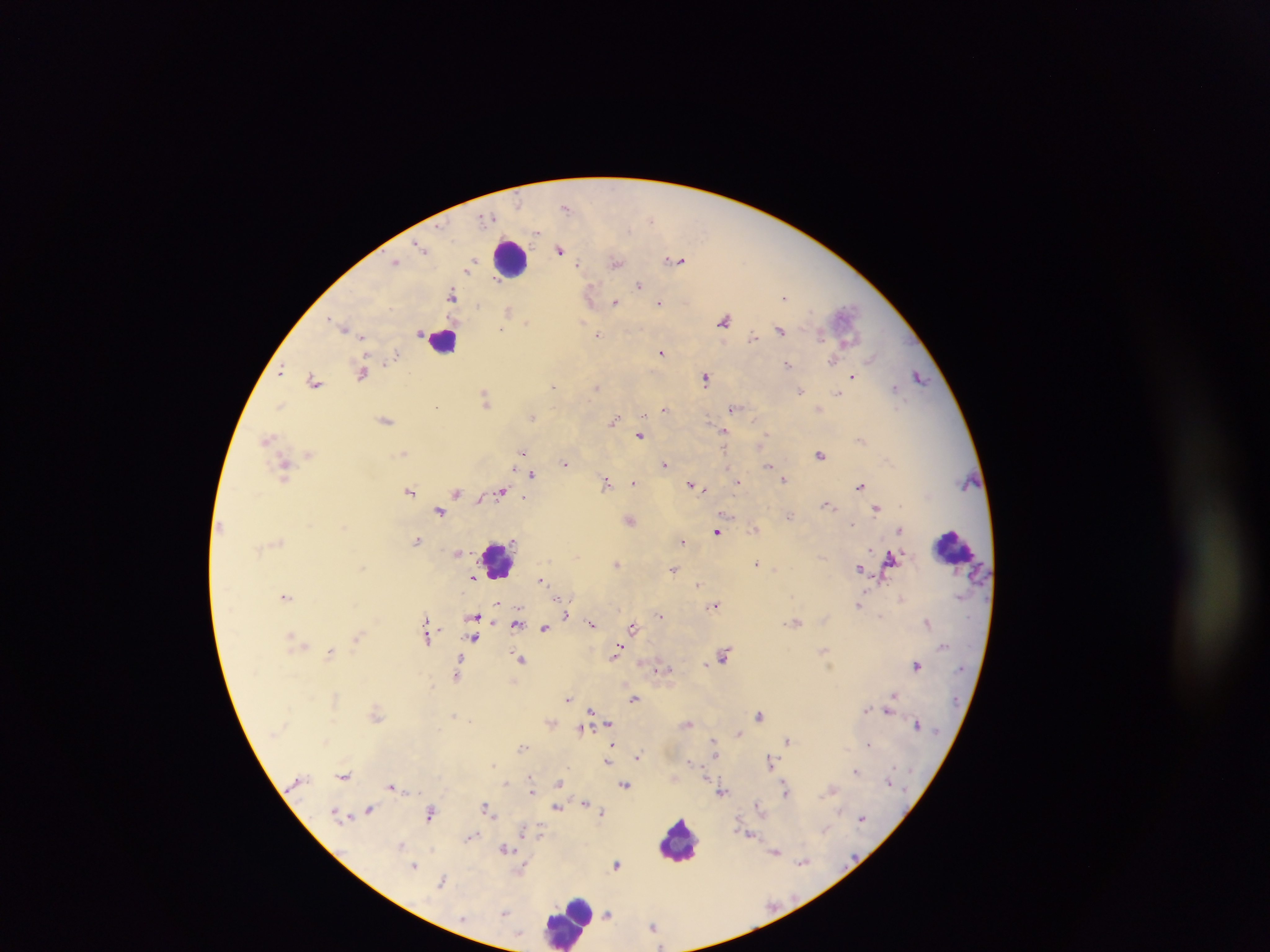

Approximate centers as [x, y] in pixels.
Summary:
  - Leukocyte locations: [510, 258], [442, 340], [953, 546], [500, 558], [680, 840], [567, 920]
  - Plasmodium parasite locations: [566, 207], [487, 216], [651, 219], [537, 233], [421, 247], [560, 250], [679, 261], [396, 262], [472, 262], [616, 262], [578, 264], [468, 270], [638, 285], [453, 295], [785, 296], [615, 302], [659, 302], [476, 305], [508, 311], [725, 320], [526, 322], [505, 323], [344, 327], [501, 329], [780, 330], [597, 334], [753, 336], [362, 337], [821, 337], [661, 352], [395, 355], [871, 359], [390, 360], [833, 361], [788, 364], [281, 371], [362, 373], [852, 376], [919, 376], [706, 378], [315, 381], [553, 387], [597, 387], [895, 388], [801, 390], [838, 393], [485, 396], [281, 405], [437, 405], [733, 407], [664, 409], [645, 416], [533, 417], [385, 420], [613, 421], [724, 432], [640, 435], [765, 437], [268, 438], [860, 440], [404, 453], [523, 453], [309, 454], [820, 454], [565, 462], [665, 464], [769, 466], [284, 469], [532, 474], [784, 479], [738, 481], [606, 483], [634, 483], [692, 485], [859, 485], [704, 489], [410, 491], [501, 491], [457, 493], [525, 497], [827, 504], [876, 507], [440, 512], [790, 515], [630, 520], [851, 524], [755, 528], [900, 529], [716, 531], [417, 540], [682, 541], [890, 560], [757, 563], [617, 564], [364, 566], [859, 568], [673, 569], [473, 577], [540, 580], [698, 584], [286, 596], [558, 600], [499, 604], [715, 604], [859, 604], [660, 614], [474, 616], [566, 616], [882, 617], [427, 620], [928, 622], [517, 623], [591, 623], [633, 627], [545, 628], [291, 636], [427, 636], [358, 637], [474, 638], [617, 651], [330, 652], [724, 655], [520, 659], [706, 664], [916, 665], [459, 667], [661, 668], [458, 674], [893, 695], [634, 698], [568, 699], [868, 709], [591, 710], [888, 712], [376, 714], [454, 715], [760, 715], [609, 723], [688, 723], [917, 724], [581, 728], [739, 733], [713, 740], [788, 740], [868, 744], [612, 745], [522, 747], [638, 755], [607, 761], [771, 761], [690, 762], [856, 771], [343, 775], [506, 782], [559, 782], [625, 784], [392, 787], [786, 789], [831, 790], [532, 791], [721, 792], [586, 803], [757, 805], [486, 807], [556, 807], [369, 809], [602, 812], [430, 813], [336, 814], [862, 818], [824, 830], [524, 831], [540, 834], [750, 835], [471, 836], [401, 845], [505, 848], [776, 853], [803, 862], [617, 864], [414, 865], [523, 869], [443, 881], [505, 912], [608, 914], [652, 925]
  - Country: Ghana
  - Capture: mobile-phone photograph through a microscope
  - Preparation: thick blood film
  - Image size: 1270×952 pixels
  - Field of view: single